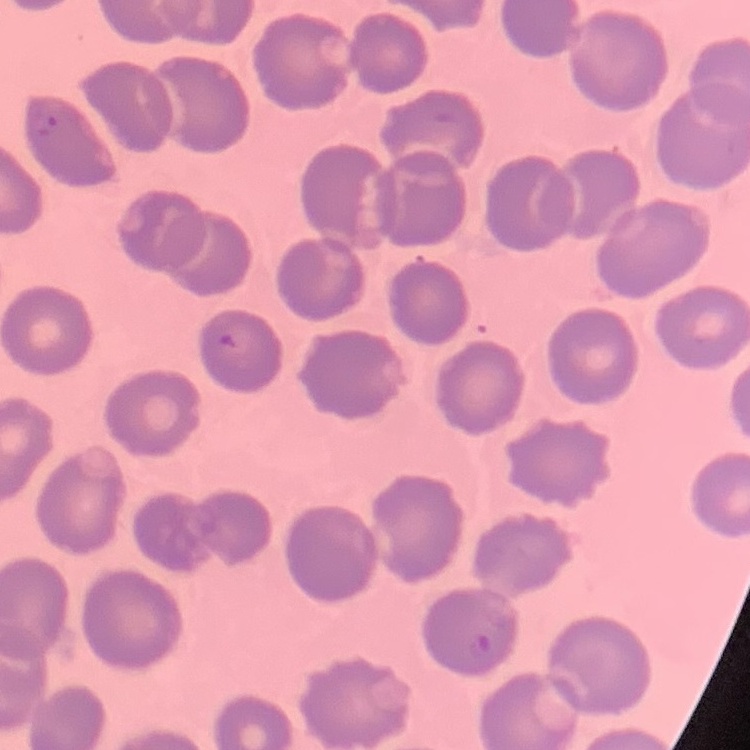

Summary:
  - Erythrocyte morphology: no rouleaux formation
  - Image type: one tile cut from a larger photomicrograph
  - Stain: Field's or Giemsa
  - Preparation: thin peripheral smear